Draw a bounding box around every leukocyte (white blood cell).
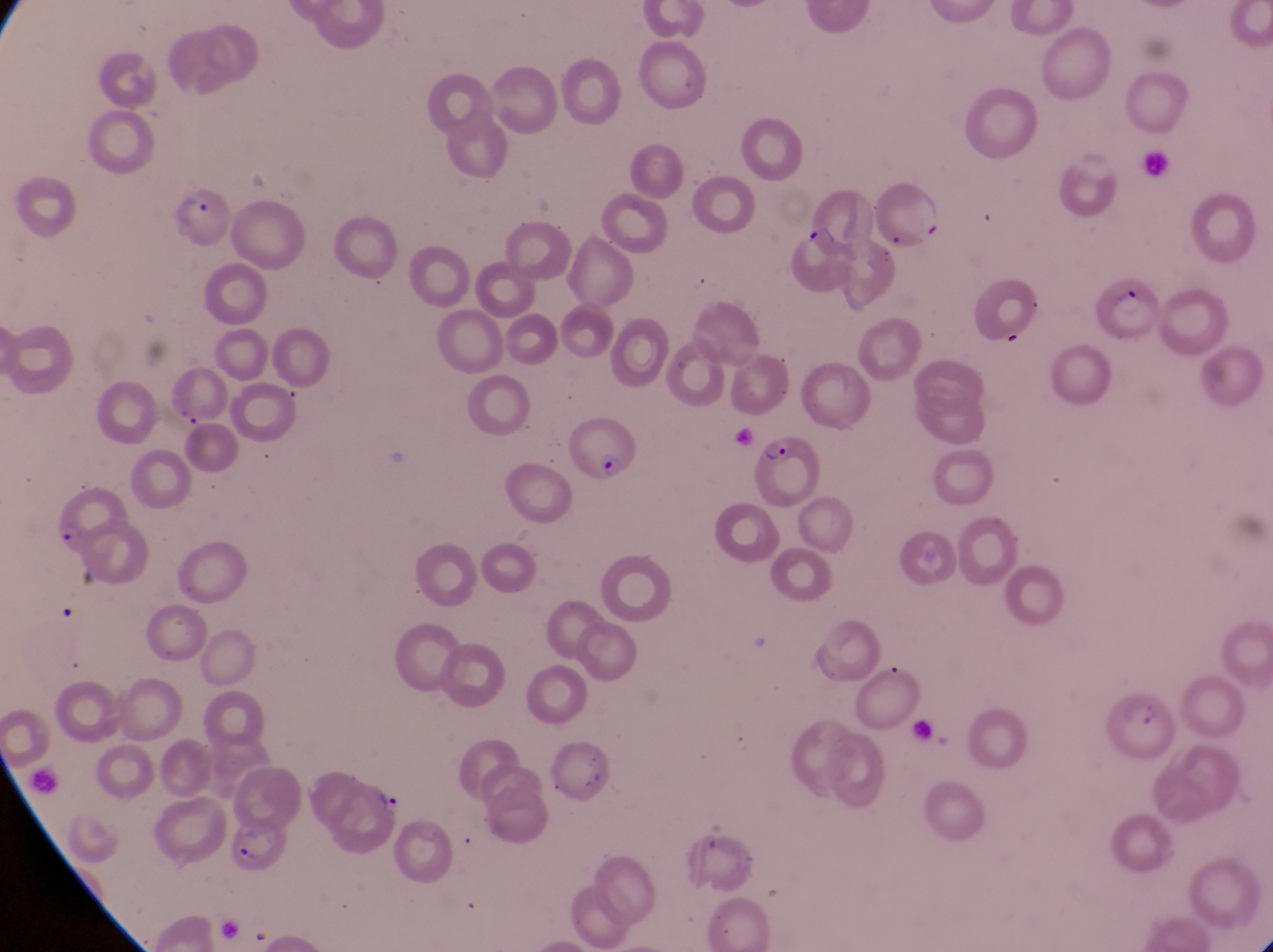

No leukocytes observed.

Approximate bounding boxes as (left, top, right, bottom) in pixels. Trophozoite locations: (370, 781, 403, 820). Parasitised red blood cell locations: (160, 180, 230, 252), (872, 181, 943, 248), (794, 185, 872, 252), (1103, 274, 1158, 337), (565, 417, 639, 484), (751, 430, 825, 512), (52, 492, 129, 550), (1103, 684, 1177, 761), (224, 814, 289, 874). Captured by a smartphone held over the eyepiece of an Olympus CX-23 microscope. Single field of view. Sample from Uganda. Magnification of 1000x. Image is 1273×952 pixels. Thin blood film.